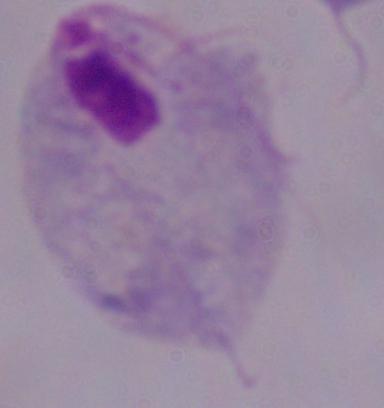

identification = trichomonad
modality = photomicrograph
magnification = 1000x